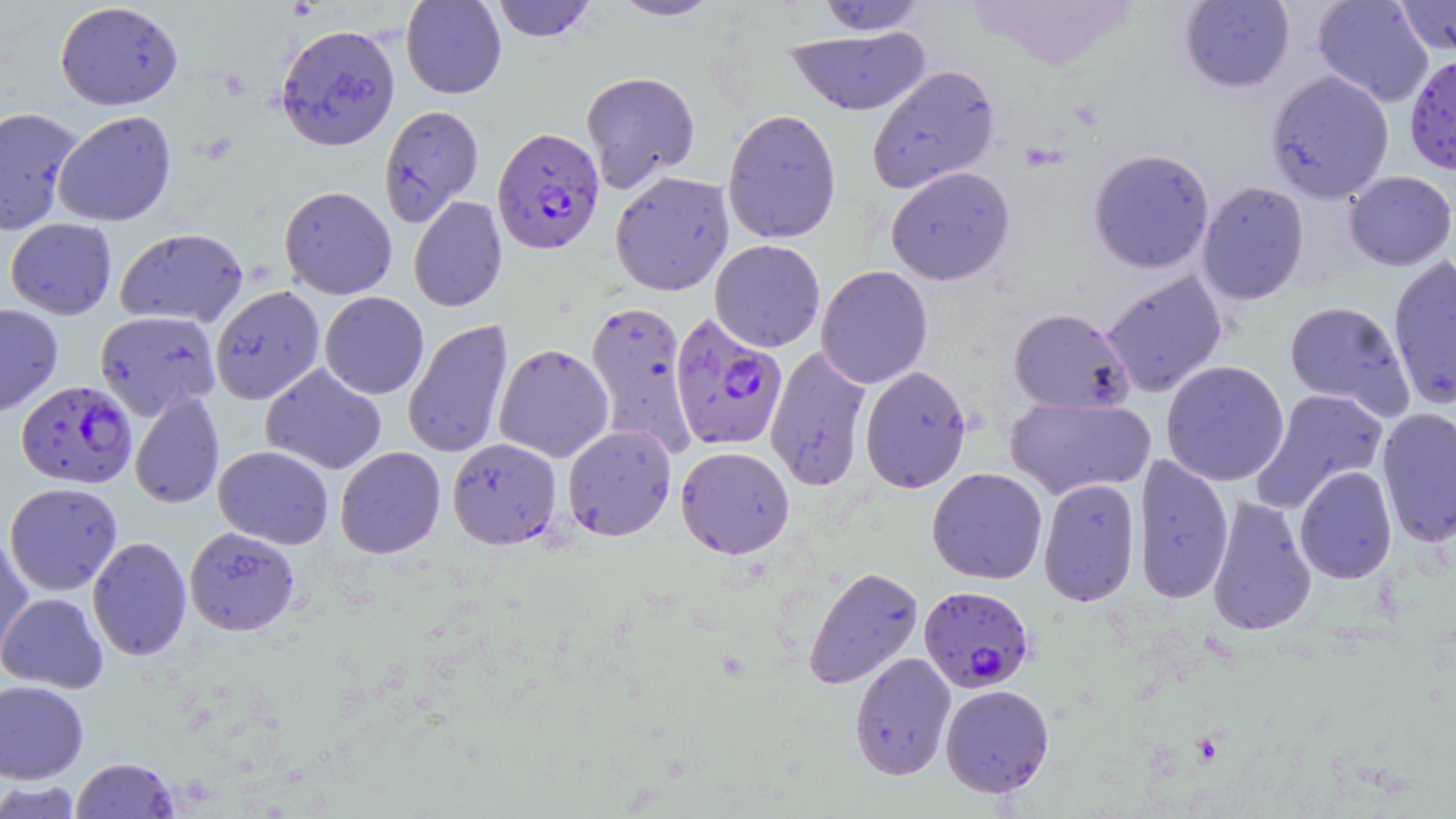

slide_level_diagnosis: Plasmodium falciparum
modality: optical microscopy
magnification: 1000x
uninfected_red_blood_cell_locations: 'approximate bounding boxes as (x1, y1, x2, y2) in pixels: (400, 0, 507, 99), (491, 0, 598, 42), (608, 0, 722, 21), (816, 0, 926, 35), (1179, 0, 1295, 93), (1312, 0, 1434, 107), (1393, 0, 1456, 57), (55, 2, 183, 110), (275, 23, 401, 152), (784, 27, 930, 116), (866, 64, 1001, 194), (1265, 70, 1395, 203), (580, 71, 701, 192), (379, 104, 484, 225), (0, 106, 83, 235), (722, 109, 841, 244), (53, 110, 177, 226), (1088, 147, 1215, 274), (886, 166, 1015, 286), (610, 170, 734, 296), (1344, 170, 1456, 270), (1197, 181, 1310, 305), (279, 185, 397, 300), (409, 196, 507, 312), (5, 218, 117, 320), (114, 227, 248, 327), (709, 239, 826, 352), (1386, 254, 1456, 410), (815, 265, 933, 389), (1101, 270, 1228, 397), (210, 285, 325, 405), (319, 292, 429, 399), (584, 300, 697, 456), (1284, 300, 1414, 418), (0, 304, 63, 416), (1008, 307, 1134, 414), (94, 311, 220, 419), (403, 318, 513, 459), (493, 343, 614, 462), (765, 345, 872, 491), (1161, 360, 1289, 487), (261, 363, 387, 475), (859, 365, 972, 493), (1252, 387, 1389, 513), (129, 390, 225, 509), (1004, 396, 1156, 500), (1376, 407, 1456, 548), (563, 424, 677, 541), (447, 438, 561, 549), (213, 445, 333, 549), (335, 446, 446, 559), (675, 446, 794, 559), (1133, 452, 1234, 604), (1294, 465, 1397, 585), (926, 467, 1048, 585), (1038, 477, 1141, 607), (4, 482, 123, 595), (1206, 494, 1317, 637), (185, 527, 299, 635), (0, 531, 35, 667), (87, 536, 191, 661), (803, 565, 924, 690), (1, 593, 108, 693), (849, 652, 956, 780), (0, 680, 89, 784), (940, 684, 1054, 798), (69, 756, 180, 818), (0, 780, 84, 818)'
field_of_view: single
image_size: 1456×819 pixels
plasmodium_falciparum_infected_red_blood_cell_locations: 'approximate bounding boxes as (x1, y1, x2, y2) in pixels: (1404, 52, 1456, 175), (492, 126, 605, 254), (669, 312, 788, 452), (16, 380, 137, 488), (919, 585, 1035, 692)'
stain: May-Grünwald-Giemsa
preparation: thin blood film